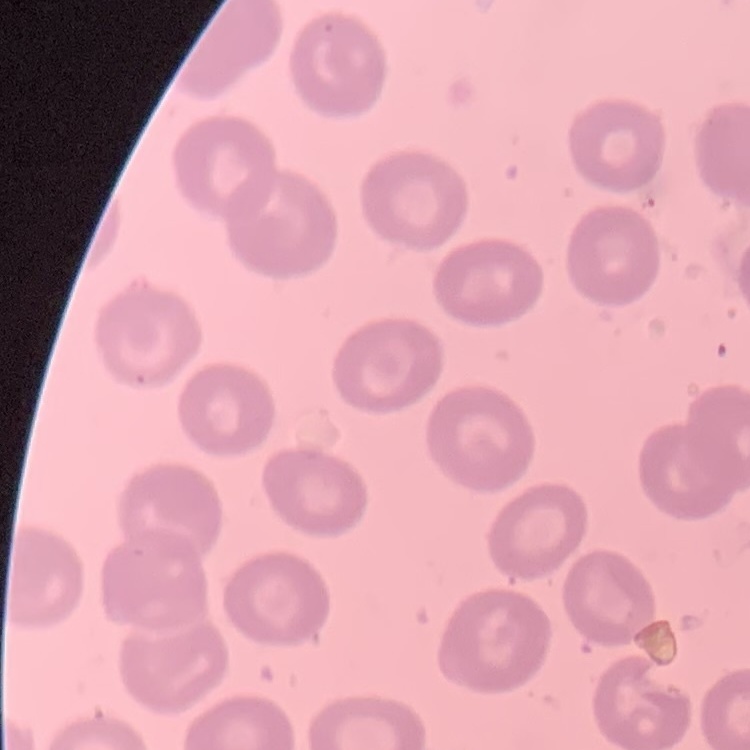
Summary:
  - Red blood cell morphology: no rouleaux formation
  - Image type: one tile cut from a larger photomicrograph
  - Stain: Field's or Giemsa
  - Preparation: thin peripheral smear